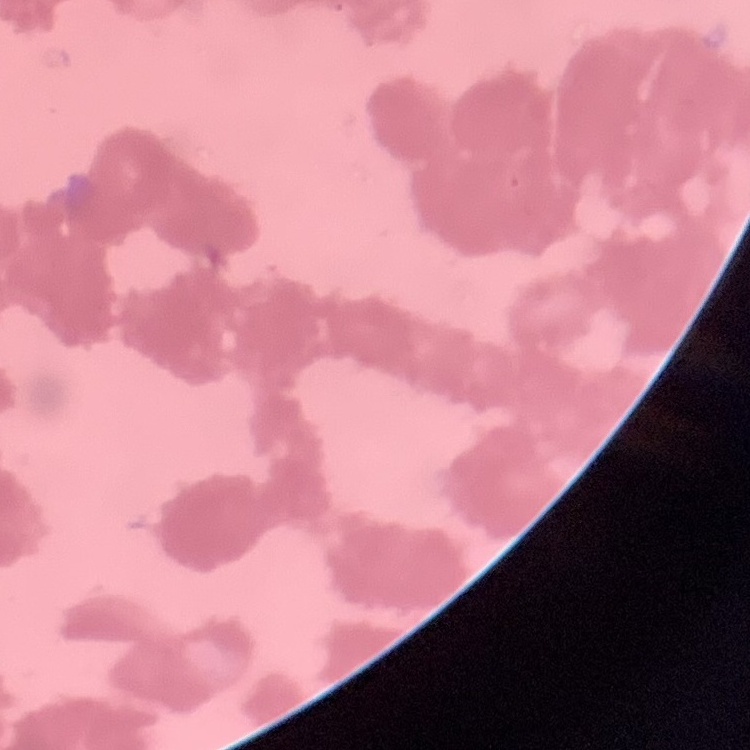
red_blood_cell_morphology: rouleaux formation
image_type: square crop of a larger photomicrograph
preparation: thin blood film
stain: Field's or Giemsa